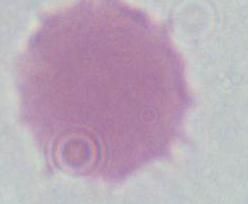

Summary:
  - Identification: erythrocyte
  - Modality: micrograph
  - Magnification: 1000x